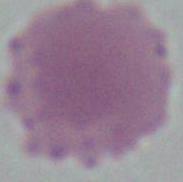

Micrograph. A red blood cell is seen. 1000x magnification.